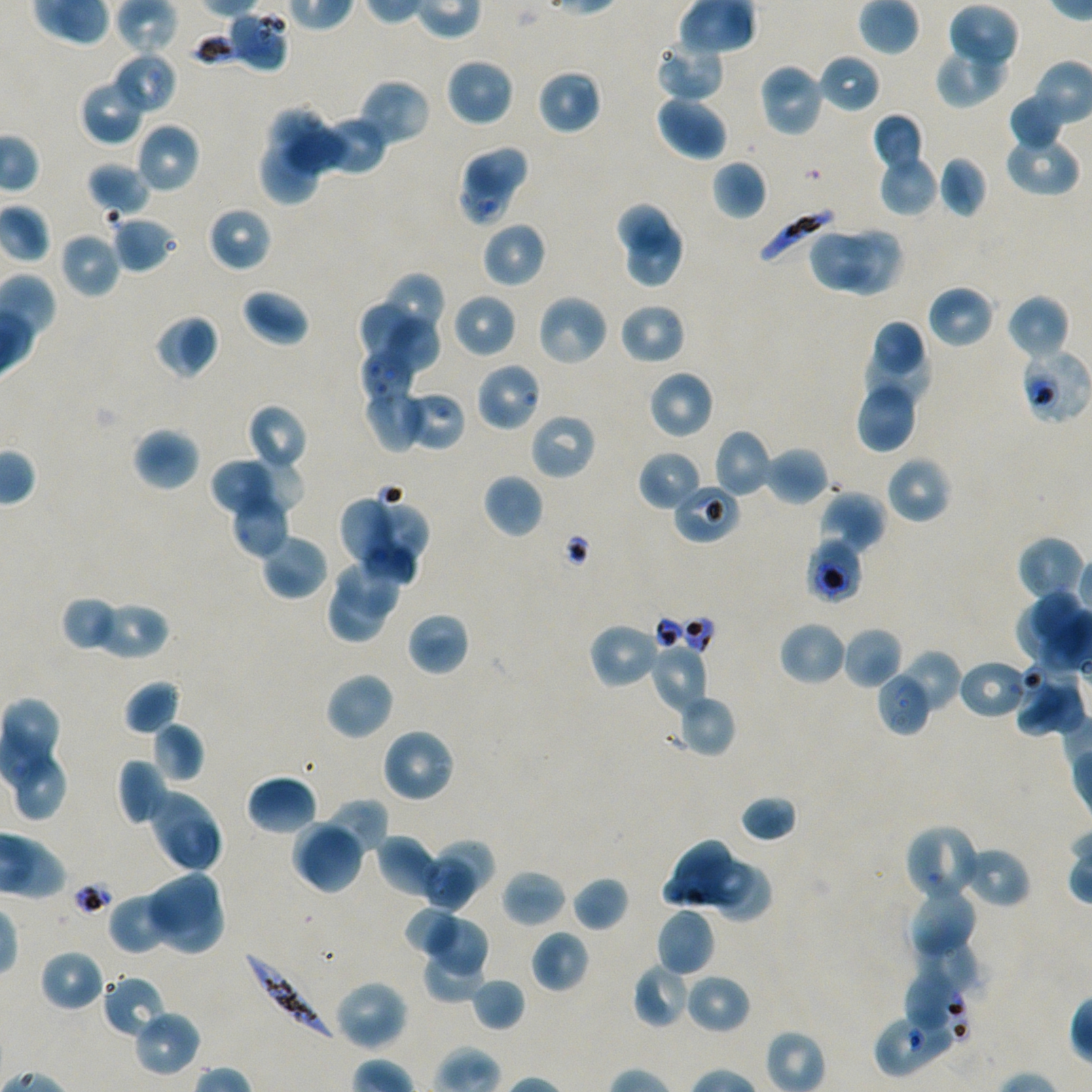 Approximate bounding rectangles given as corner coordinates in pixels from the top-left. Not every red blood cell is marked. A life-cycle stage — or a range of stages, where the recorded stages span more than one — follows each staged infected red blood cell. Locations of uninfected red blood cells: (x1=947, y1=4, x2=1019, y2=71), (x1=655, y1=38, x2=725, y2=102), (x1=935, y1=44, x2=1008, y2=108), (x1=112, y1=52, x2=177, y2=115), (x1=818, y1=54, x2=880, y2=113), (x1=445, y1=56, x2=515, y2=127), (x1=757, y1=62, x2=826, y2=138), (x1=536, y1=68, x2=602, y2=136), (x1=79, y1=77, x2=147, y2=145), (x1=356, y1=79, x2=431, y2=147), (x1=655, y1=94, x2=728, y2=160), (x1=1008, y1=94, x2=1066, y2=151), (x1=266, y1=105, x2=329, y2=164), (x1=872, y1=113, x2=924, y2=173), (x1=322, y1=117, x2=388, y2=176), (x1=134, y1=122, x2=201, y2=194), (x1=286, y1=126, x2=345, y2=173), (x1=1004, y1=131, x2=1080, y2=196), (x1=460, y1=143, x2=531, y2=197), (x1=259, y1=145, x2=323, y2=204), (x1=878, y1=152, x2=939, y2=217), (x1=938, y1=155, x2=988, y2=218), (x1=711, y1=160, x2=768, y2=220), (x1=87, y1=162, x2=151, y2=217), (x1=614, y1=201, x2=674, y2=256), (x1=206, y1=206, x2=272, y2=272), (x1=111, y1=216, x2=177, y2=273), (x1=481, y1=221, x2=547, y2=288), (x1=624, y1=223, x2=687, y2=289), (x1=843, y1=225, x2=904, y2=295), (x1=807, y1=228, x2=873, y2=291), (x1=58, y1=231, x2=121, y2=298), (x1=377, y1=272, x2=447, y2=345), (x1=927, y1=285, x2=994, y2=348), (x1=242, y1=288, x2=310, y2=346), (x1=451, y1=293, x2=517, y2=359), (x1=1006, y1=293, x2=1070, y2=361), (x1=536, y1=294, x2=608, y2=367), (x1=360, y1=299, x2=416, y2=363), (x1=619, y1=302, x2=686, y2=365), (x1=155, y1=314, x2=219, y2=379), (x1=385, y1=318, x2=441, y2=378), (x1=875, y1=320, x2=923, y2=371), (x1=865, y1=346, x2=932, y2=407), (x1=647, y1=369, x2=714, y2=439), (x1=856, y1=379, x2=920, y2=453), (x1=363, y1=383, x2=426, y2=452), (x1=247, y1=403, x2=308, y2=473), (x1=530, y1=413, x2=596, y2=480), (x1=132, y1=427, x2=201, y2=491), (x1=712, y1=429, x2=773, y2=498), (x1=764, y1=445, x2=829, y2=505), (x1=638, y1=450, x2=703, y2=511), (x1=252, y1=452, x2=306, y2=514), (x1=885, y1=456, x2=952, y2=524), (x1=209, y1=460, x2=271, y2=518), (x1=482, y1=473, x2=544, y2=539), (x1=672, y1=481, x2=741, y2=544), (x1=818, y1=490, x2=886, y2=554), (x1=230, y1=492, x2=290, y2=558), (x1=342, y1=496, x2=396, y2=565), (x1=371, y1=499, x2=429, y2=569), (x1=259, y1=534, x2=329, y2=600), (x1=1016, y1=535, x2=1086, y2=605), (x1=363, y1=536, x2=418, y2=586), (x1=337, y1=558, x2=401, y2=620), (x1=329, y1=585, x2=388, y2=642), (x1=1013, y1=591, x2=1082, y2=663), (x1=60, y1=596, x2=124, y2=654), (x1=91, y1=600, x2=169, y2=660), (x1=406, y1=611, x2=470, y2=676), (x1=778, y1=621, x2=848, y2=686), (x1=588, y1=622, x2=661, y2=689), (x1=841, y1=626, x2=903, y2=690), (x1=651, y1=646, x2=708, y2=714), (x1=899, y1=649, x2=962, y2=713), (x1=1012, y1=669, x2=1078, y2=739), (x1=325, y1=672, x2=395, y2=740), (x1=124, y1=679, x2=181, y2=735), (x1=674, y1=693, x2=737, y2=758), (x1=151, y1=721, x2=204, y2=783), (x1=380, y1=727, x2=456, y2=803), (x1=117, y1=758, x2=169, y2=827), (x1=247, y1=774, x2=317, y2=835), (x1=146, y1=786, x2=224, y2=874), (x1=740, y1=795, x2=798, y2=843), (x1=318, y1=798, x2=388, y2=860), (x1=290, y1=816, x2=358, y2=885), (x1=304, y1=829, x2=365, y2=894), (x1=375, y1=836, x2=443, y2=901), (x1=435, y1=838, x2=494, y2=896), (x1=663, y1=839, x2=730, y2=907), (x1=962, y1=850, x2=1027, y2=904), (x1=418, y1=858, x2=477, y2=916), (x1=703, y1=858, x2=752, y2=908), (x1=715, y1=864, x2=773, y2=920), (x1=501, y1=868, x2=567, y2=928), (x1=145, y1=871, x2=220, y2=930), (x1=570, y1=875, x2=630, y2=932), (x1=905, y1=884, x2=977, y2=961), (x1=108, y1=890, x2=179, y2=954), (x1=156, y1=892, x2=225, y2=956), (x1=407, y1=909, x2=458, y2=954), (x1=656, y1=909, x2=715, y2=977), (x1=426, y1=915, x2=491, y2=975), (x1=530, y1=930, x2=590, y2=993), (x1=917, y1=939, x2=982, y2=996), (x1=39, y1=949, x2=105, y2=1012), (x1=422, y1=954, x2=484, y2=1002), (x1=632, y1=962, x2=693, y2=1029), (x1=684, y1=973, x2=750, y2=1034), (x1=101, y1=975, x2=166, y2=1040), (x1=470, y1=977, x2=526, y2=1032), (x1=333, y1=979, x2=408, y2=1051), (x1=132, y1=1009, x2=202, y2=1078). Locations of infected red blood cells: (x1=756, y1=207, x2=835, y2=267); (x1=1019, y1=347, x2=1091, y2=425) early trophozoite; (x1=244, y1=949, x2=338, y2=1041). Locations of red blood cells of indeterminate infection status: (x1=228, y1=10, x2=289, y2=71), (x1=456, y1=156, x2=513, y2=227), (x1=359, y1=348, x2=416, y2=404), (x1=475, y1=362, x2=543, y2=433), (x1=405, y1=391, x2=466, y2=452), (x1=806, y1=539, x2=864, y2=604), (x1=958, y1=659, x2=1030, y2=719), (x1=875, y1=669, x2=934, y2=736), (x1=904, y1=823, x2=983, y2=903), (x1=904, y1=968, x2=967, y2=1030), (x1=873, y1=1007, x2=960, y2=1077). Giemsa stain. 100x oil-immersion objective, numerical aperture 1.45. Image is 1092×1092 pixels. Donor blood group A+/O+. Single field of view. Thin blood smear. P. falciparum strain NF54 maintained in static in-vitro culture.